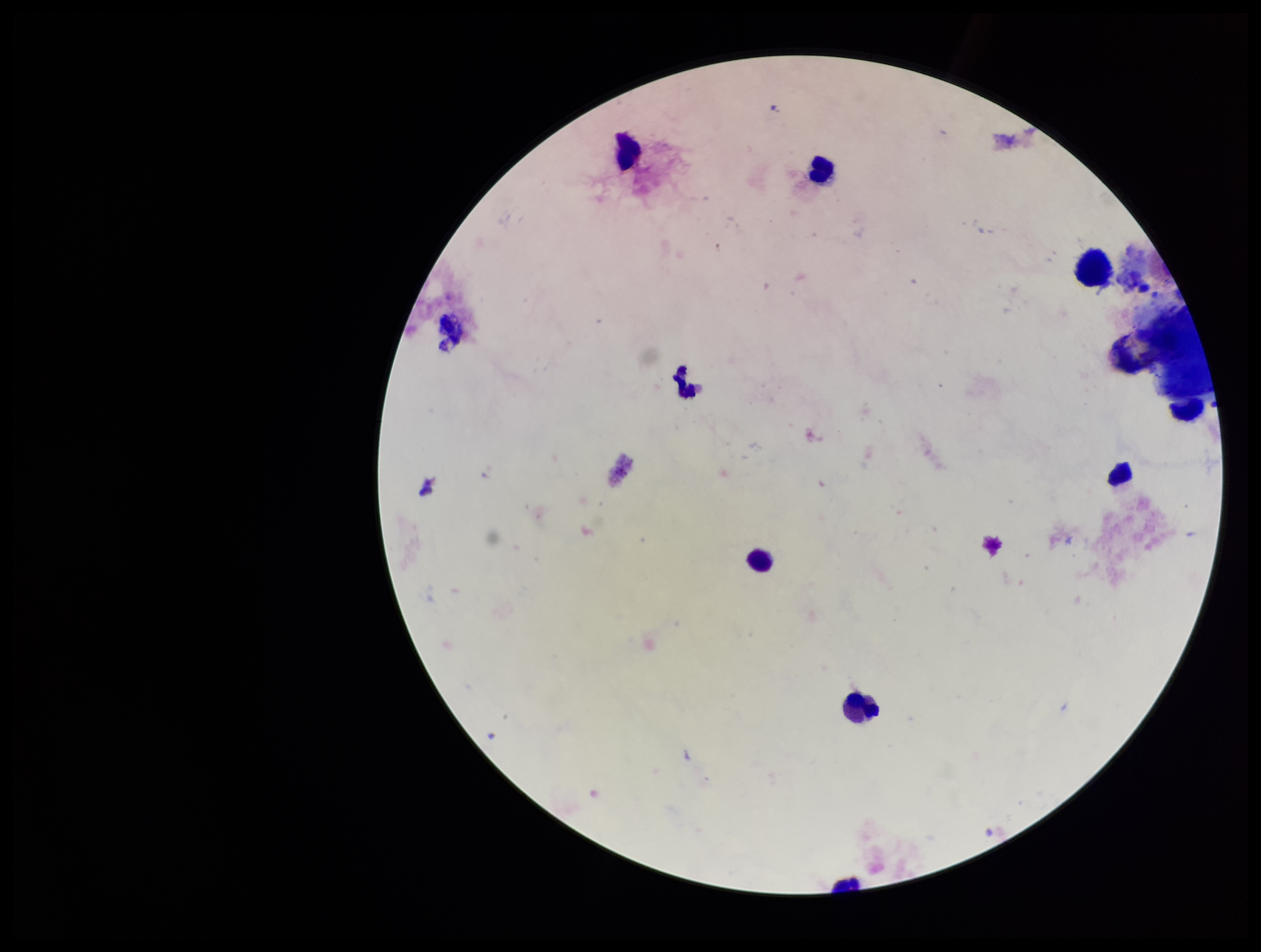

preparation = thick smear
patient malaria status = negative
capture = smartphone photograph through the microscope eyepiece
image size = 1261×952 pixels
stain = Giemsa
field of view = single
leukocyte count = 9
parasite count = 0
Plasmodium parasites = none detected